Classify this cell by malaria status.
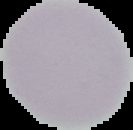
Uninfected.

Image is 133×130 pixels. Cell region segmented out of the field of view; the surrounding area is masked to black. From a thin blood smear.